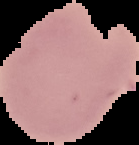
Result: negative for malaria parasites. From a thin blood smear. Image is 139×145 pixels. Cell region segmented out of the field of view; the surrounding area is masked to black.